Give the position of every Plasmodium parasite.
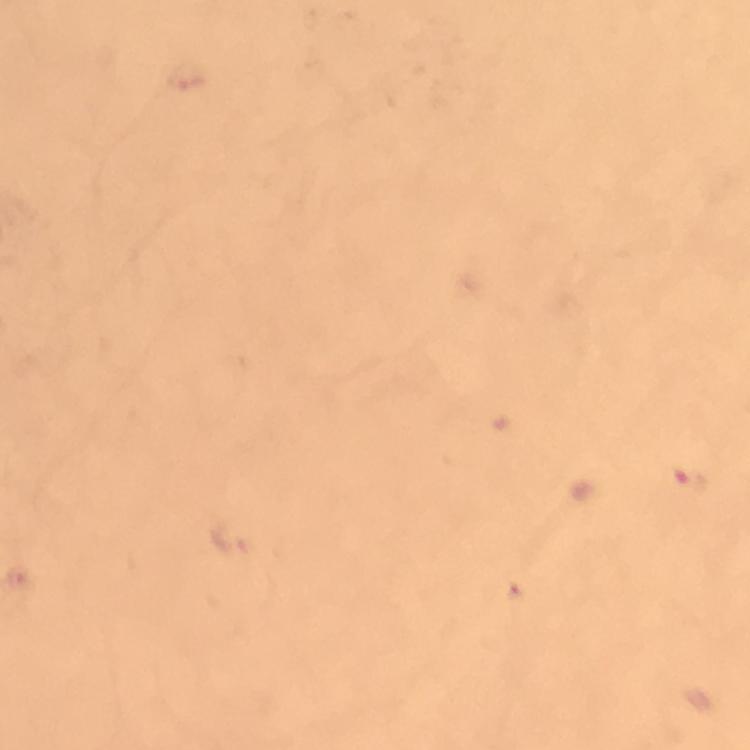

Approximate centers as {x, y} in pixels.
Plasmodium parasites: {685, 481}.

At 100x magnification. Giemsa stain. Thick blood film. From a malaria diagnostic workup. Image is 750×750 pixels. A crop from one field of view. Immersion oil applied. Smartphone photograph taken through a microscope.